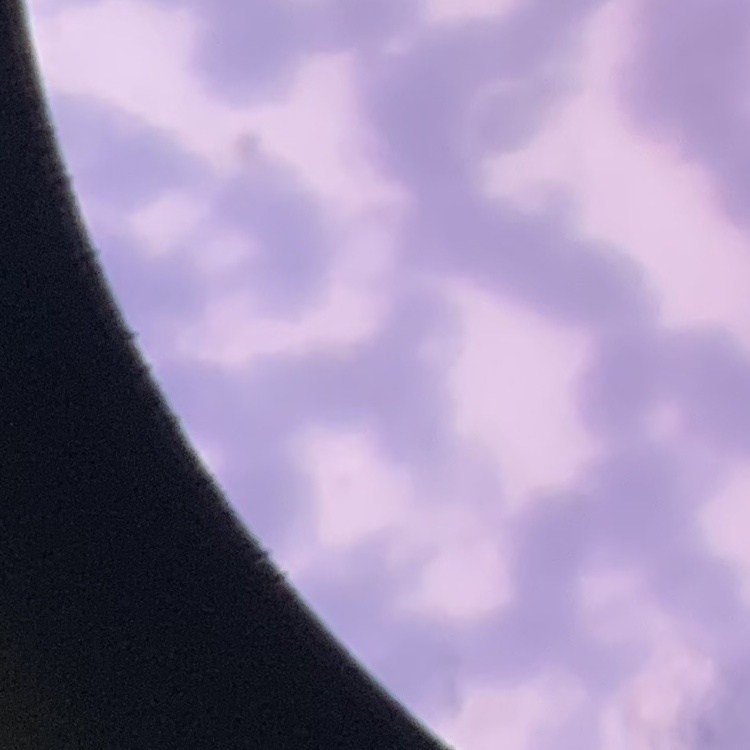

Summary:
  - Erythrocyte morphology: rouleaux formation
  - Preparation: thin blood smear
  - Stain: Field's or Giemsa
  - Image type: square crop of a larger photomicrograph